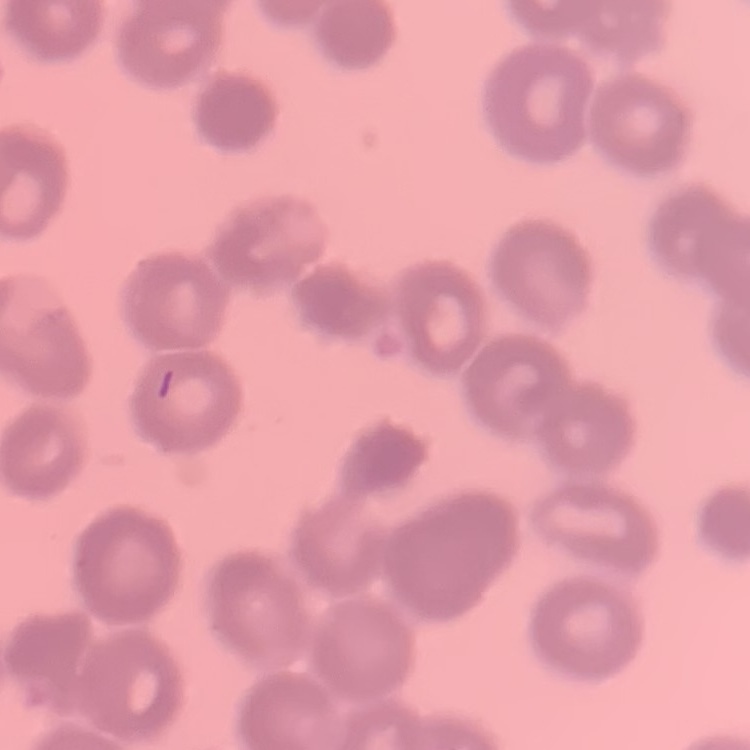
Summary:
  - Red blood cell morphology: rouleaux formation
  - Stain: Field's or Giemsa
  - Preparation: thin peripheral smear
  - Image type: square crop of a larger photomicrograph